Classify this cell by malaria status.
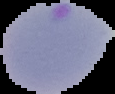

It is parasitized.

Image is 115×94 pixels. From a thin blood film. Cell region segmented out of the field of view; the surrounding area is masked to black.